Evaluate for Plasmodium parasites.
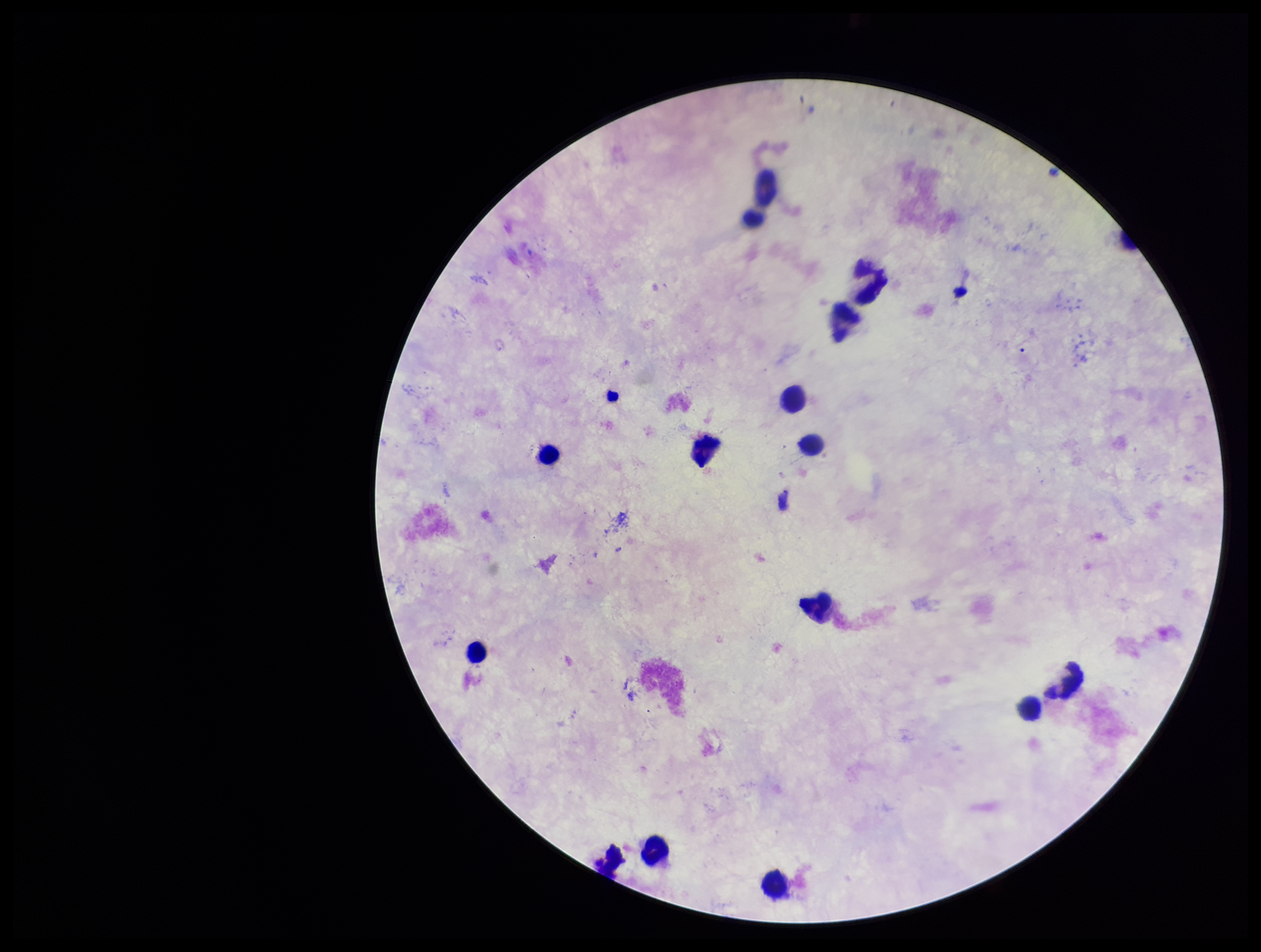
None detected.

field of view = one from this slide
parasite count = 0
leukocyte count = 14
preparation = thick smear
stain = Giemsa
capture = smartphone photograph through the microscope eyepiece
image size = 1261×952 pixels
patient malaria status = negative